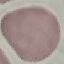

Summary:
  - Result: no malaria parasites seen
  - Stain: Giemsa
  - Image type: automatically extracted cell patch, resized to 64 × 64 pixels
  - Capture: smartphone camera at the microscope eyepiece
  - Preparation: thin smear